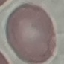
result = no malaria parasites detected
stain = Giemsa
preparation = thin smear
image type = cell patch, automatically extracted from a larger field of view and resized to 64 × 64 pixels
capture = smartphone through the microscope eyepiece